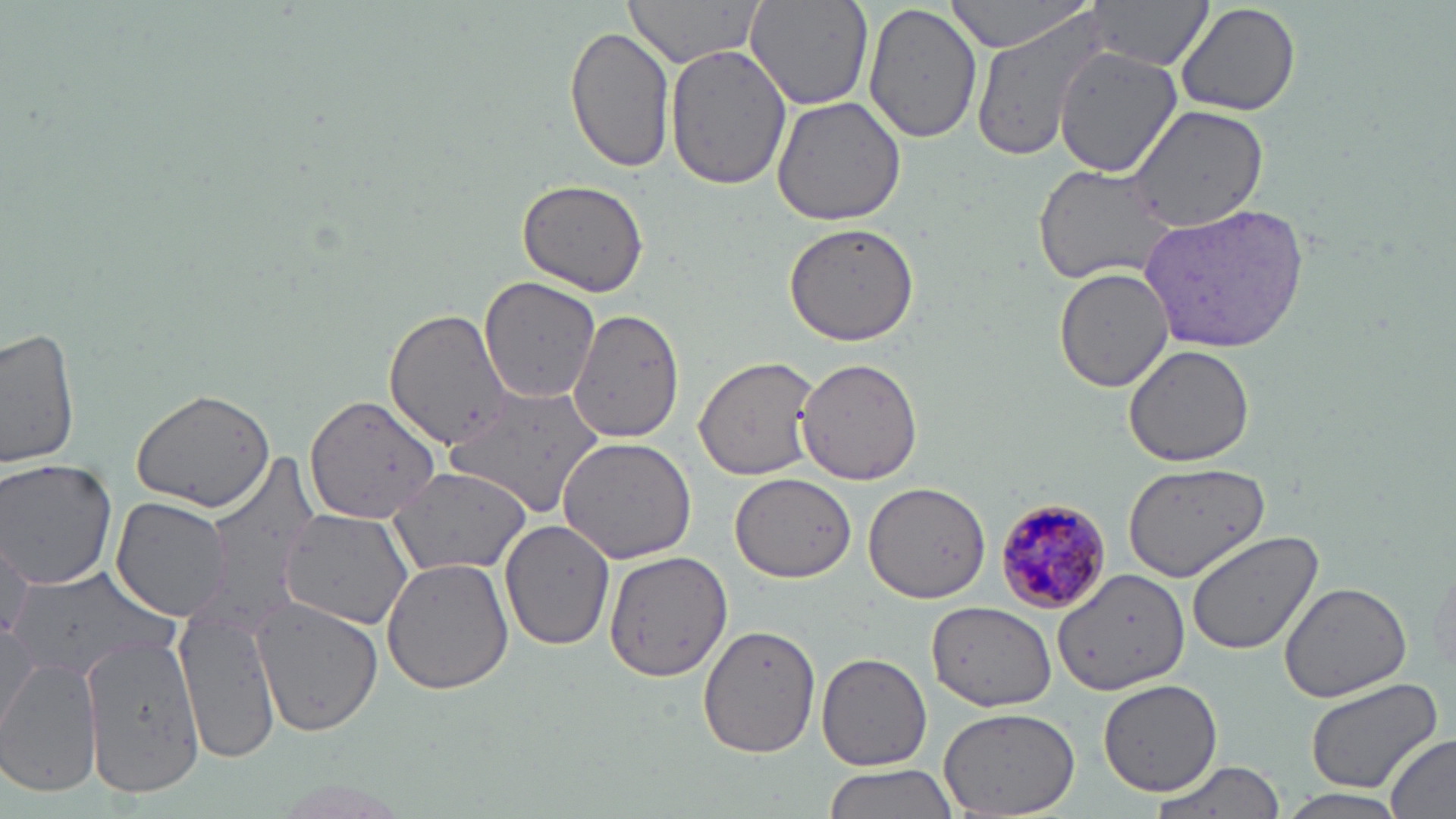

Plasmodium malariae-infected red blood cell locations = approximate bounding boxes as (x1, y1, x2, y2) in pixels: (990, 496, 1113, 618)
slide-level diagnosis = Plasmodium malariae
modality = optical microscopy
uninfected red blood cell locations = approximate bounding boxes as (x1, y1, x2, y2) in pixels: (621, 0, 764, 69), (744, 0, 873, 110), (940, 0, 1101, 53), (1173, 0, 1301, 117), (863, 1, 982, 145), (1089, 2, 1209, 68), (968, 7, 1121, 166), (565, 24, 677, 176), (666, 43, 791, 191), (1053, 44, 1180, 177), (771, 98, 907, 226), (1127, 104, 1270, 233), (1032, 163, 1179, 285), (517, 178, 652, 296), (1139, 201, 1312, 353), (782, 222, 920, 347), (1054, 268, 1176, 393), (478, 277, 602, 406), (569, 307, 685, 441), (385, 309, 511, 451), (1, 328, 82, 473), (1122, 343, 1255, 466), (694, 355, 819, 480), (795, 357, 926, 484), (443, 385, 608, 515), (131, 389, 276, 512), (305, 392, 444, 523), (557, 436, 697, 565), (199, 458, 327, 630), (0, 459, 119, 591), (1124, 461, 1269, 583), (387, 466, 530, 577), (729, 472, 856, 582), (864, 480, 989, 605), (111, 497, 231, 621), (280, 508, 415, 629), (501, 517, 615, 649), (1187, 529, 1324, 654), (1, 538, 33, 652), (604, 551, 732, 683), (1425, 551, 1456, 682), (379, 553, 515, 693), (9, 566, 175, 681), (1051, 568, 1188, 697), (1277, 579, 1412, 703), (252, 600, 382, 737), (926, 600, 1058, 712), (175, 610, 281, 763), (0, 619, 41, 735), (698, 624, 821, 758), (81, 630, 204, 801), (816, 652, 933, 771), (0, 654, 101, 798), (1301, 676, 1444, 794), (1097, 678, 1223, 795), (937, 705, 1083, 819), (1382, 736, 1456, 819), (1146, 758, 1283, 819), (821, 764, 956, 819), (1278, 788, 1411, 818)
field of view = one of a larger specimen
magnification = 1000x
stain = May-Grünwald-Giemsa
image size = 1456×819 pixels
preparation = thin blood film